Report the malaria status of this cell.
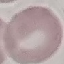
Uninfected.

Automatically extracted cell patch, resized to 64 × 64 pixels. Photographed with a smartphone camera at the microscope eyepiece. Giemsa-stained preparation. Thin blood smear.